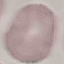
Result: no malaria parasites detected. Automatically extracted cell patch, resized to 64 × 64 pixels. Giemsa stain. Thin blood smear. Photographed with a smartphone camera at the microscope eyepiece.